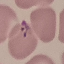

Summary:
  - Result: malaria parasites detected
  - Capture: smartphone through the microscope eyepiece
  - Image type: cell patch, automatically extracted from a larger field of view and resized to 64 × 64 pixels
  - Preparation: thin blood film
  - Stain: Giemsa